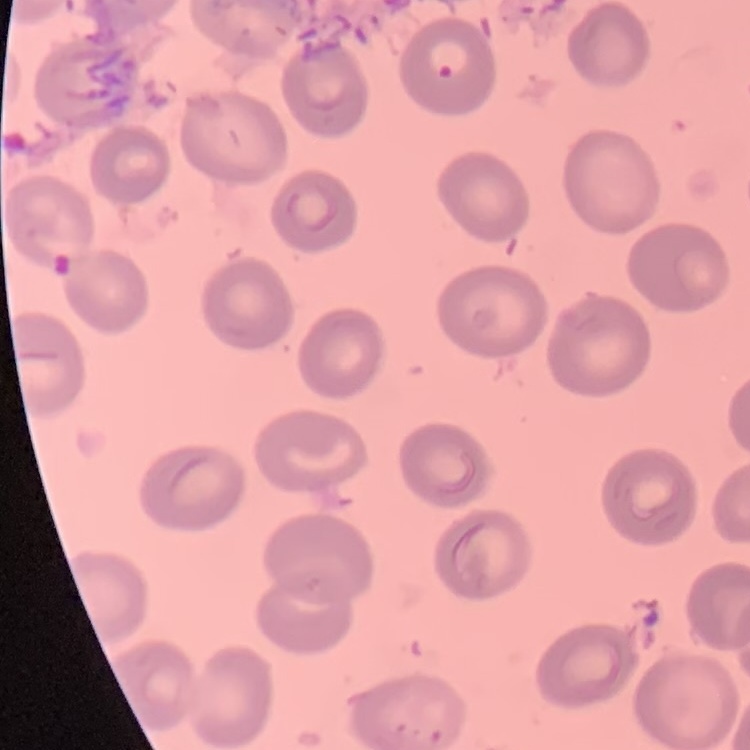 The red blood cells show no rouleaux formation. Field's or Giemsa stain. Square crop of a larger photomicrograph. Thin peripheral smear.